Assess for malaria.
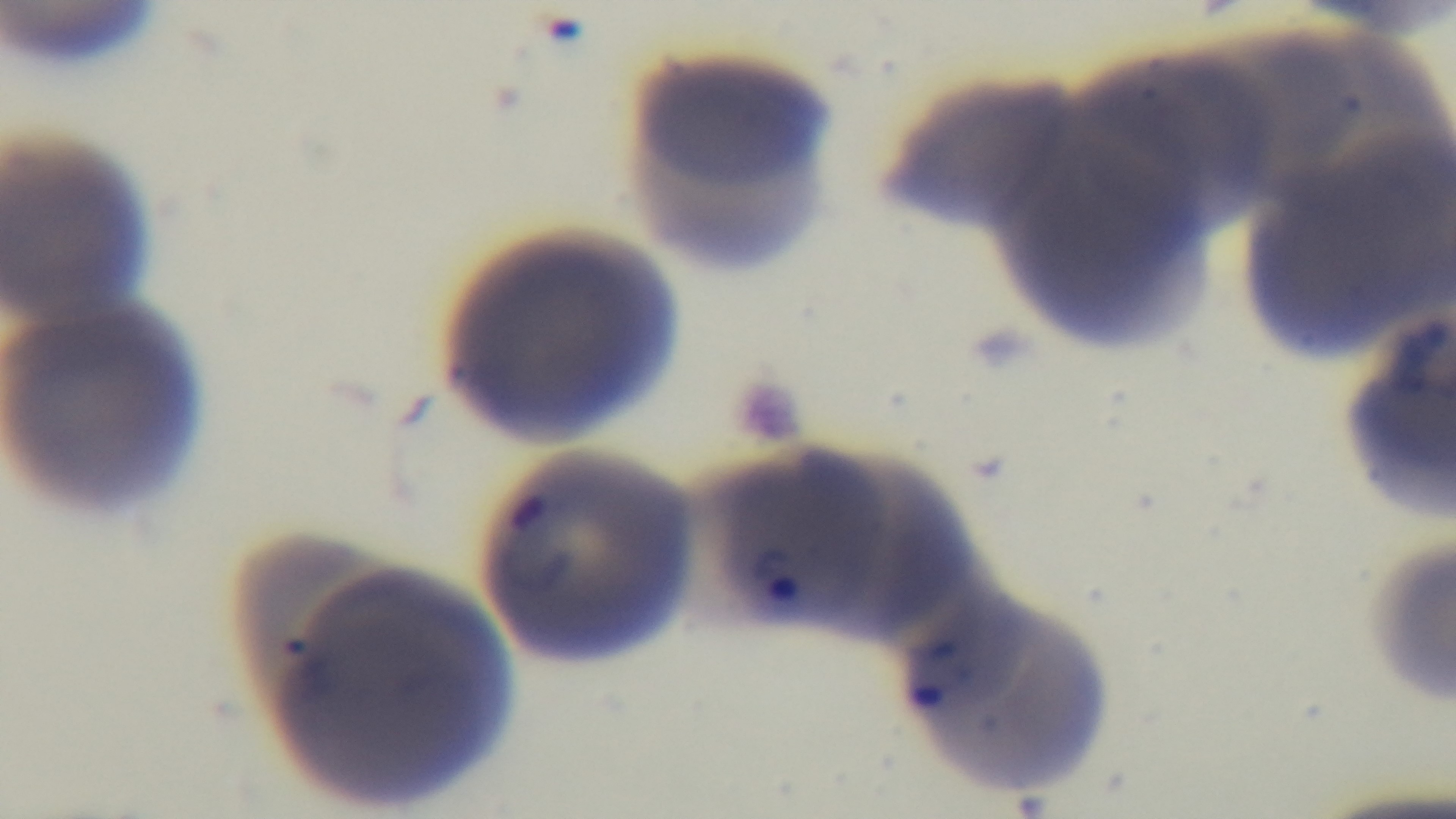

Positive.

field of view = one from the slide
objective = 100x oil immersion
modality = light microscopy
stain = Giemsa
preparation = thin smear
capture = mounted 4K digital camera